Locate every Plasmodium parasite.
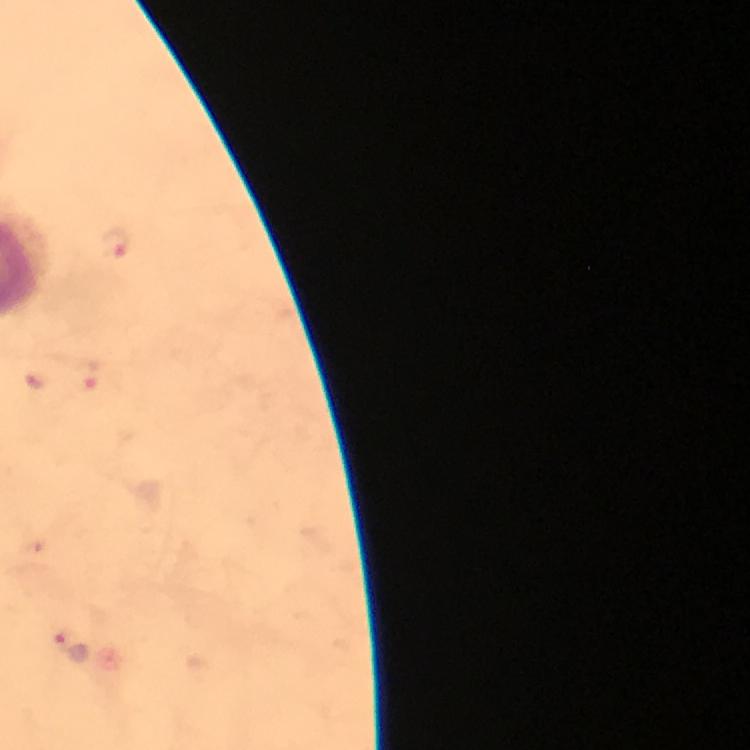

Approximate centers as [x, y] in pixels.
Plasmodium parasites: [117, 244], [69, 647].

Summary:
  - Immersion oil: applied
  - Preparation: thick blood smear
  - Image size: 750×750 pixels
  - Context: from a malaria diagnostic workup
  - Stain: Giemsa
  - Capture: smartphone mounted on the microscope
  - Cropped from: one field of view
  - Magnification: 100x